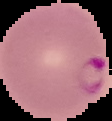

Image is 112×121 pixels. Malaria status: parasitized. The area outside the segmented cell region is set to black. From a thin blood smear.